Evaluate for parasitized red blood cells.
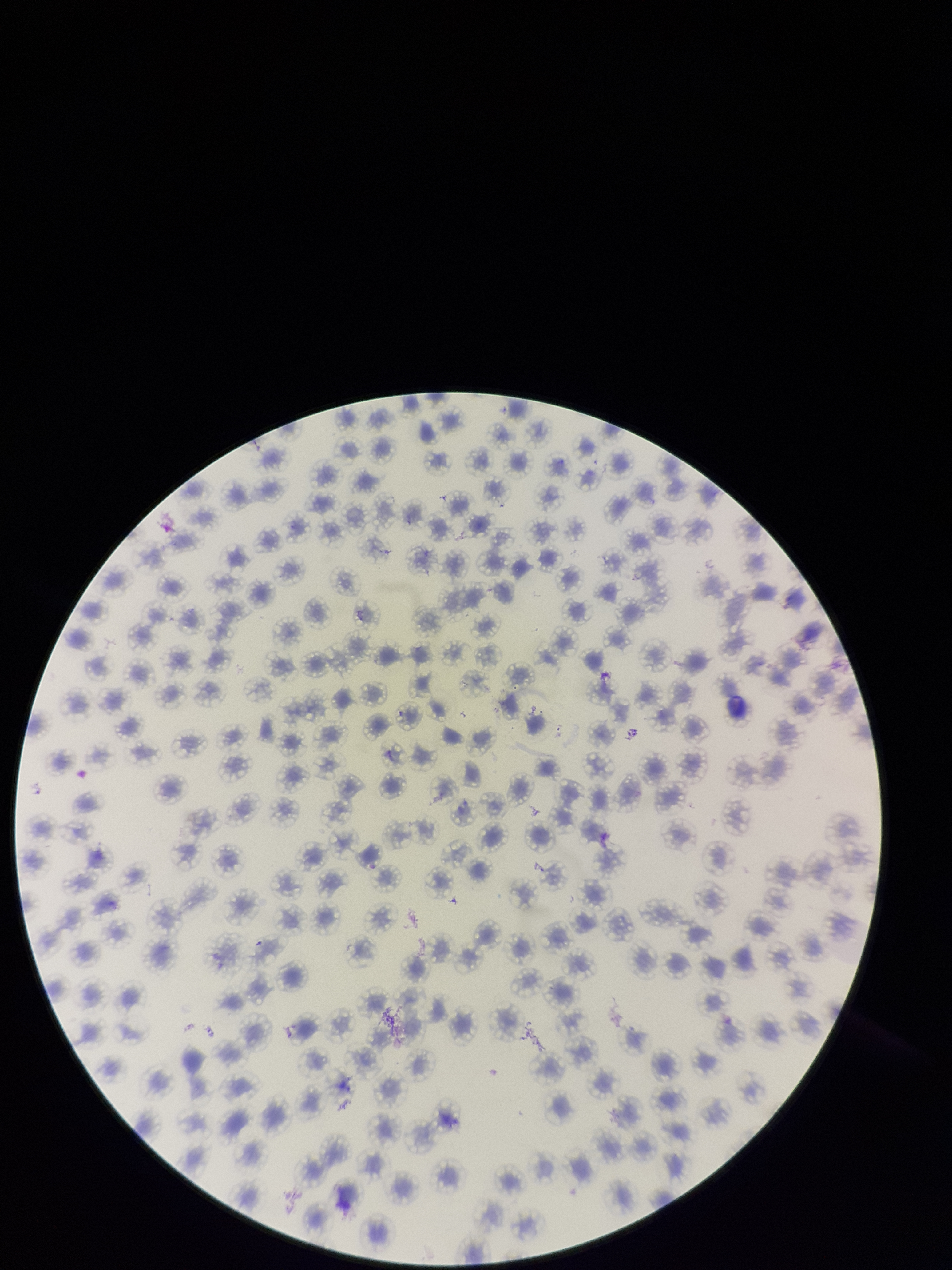

None identified.

field of view = one from this slide
red blood cell count = 157
species reported for this patient = Plasmodium falciparum
image size = 952×1270 pixels
patient malaria status = infected
preparation = thin
capture = smartphone photograph through the microscope eyepiece
parasitized red blood cell count = 0
stain = Giemsa